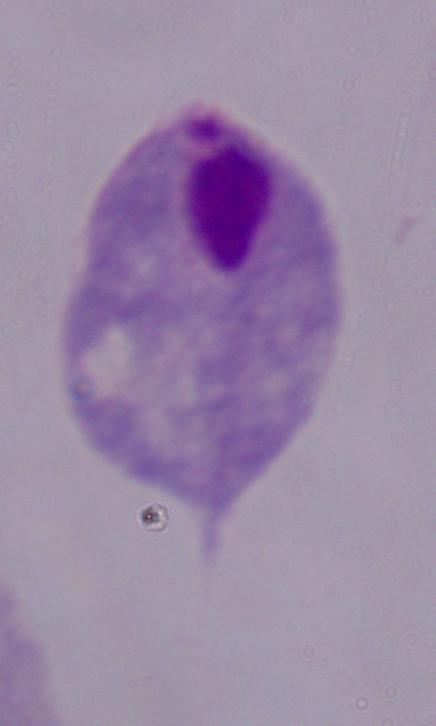

A trichomonad is seen. Captured at 1000x magnification. Micrograph.